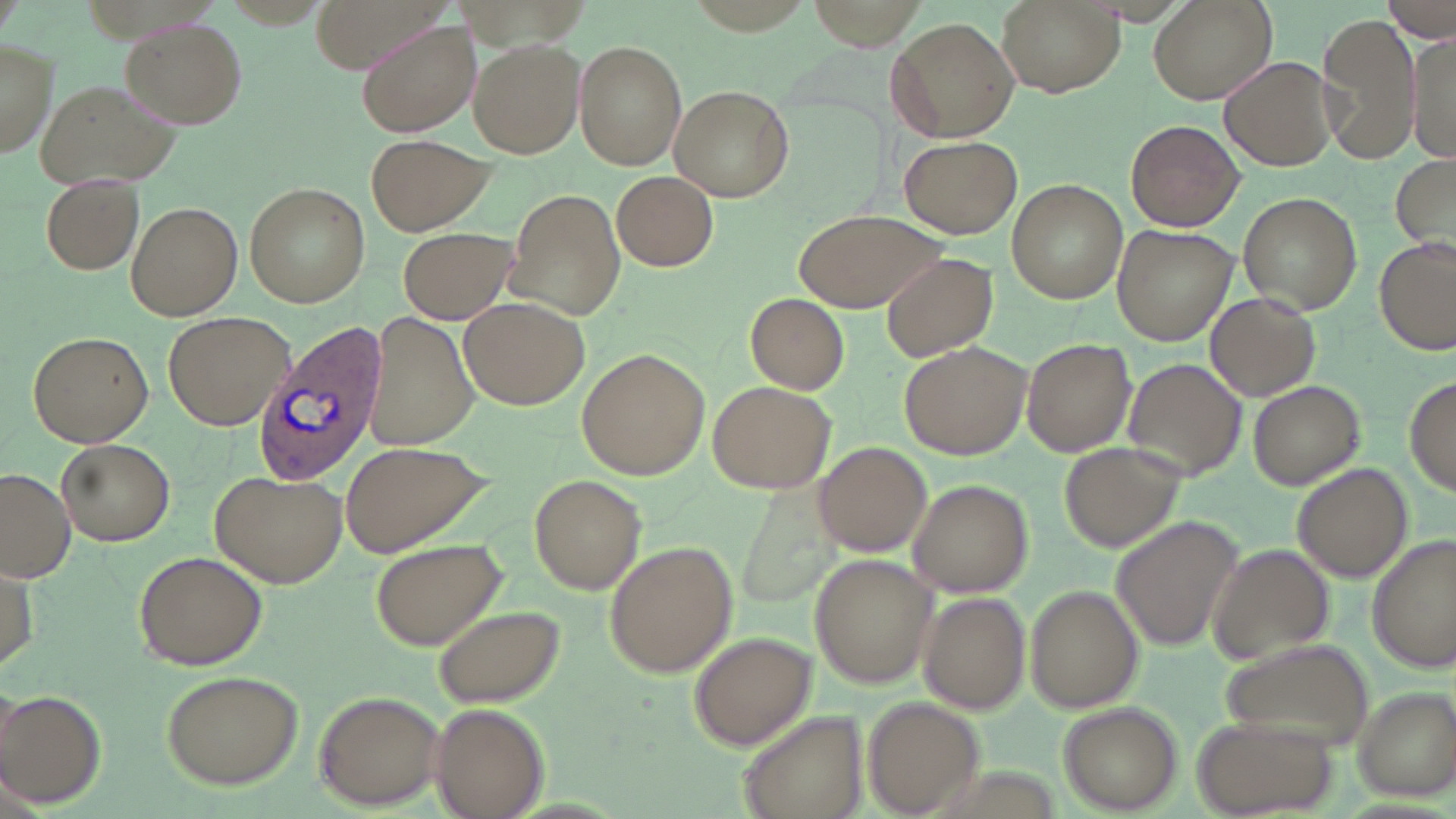

Summary:
  - Coordinate format: approximate bounding boxes as (x1,y1)-(x2,y2) corner pairs in pixels
  - Plasmodium ovale-infected red blood cell locations: (252,318)-(387,480)
  - Uninfected red blood cell locations: (308,0)-(450,75), (1147,0)-(1278,105), (1383,0)-(1455,44), (997,1)-(1123,97), (1317,11)-(1421,166), (886,16)-(1022,143), (123,17)-(247,128), (354,19)-(481,140), (1408,34)-(1454,164), (1,38)-(58,161), (467,38)-(587,159), (573,39)-(688,172), (1220,57)-(1337,172), (33,79)-(186,188), (668,85)-(794,202), (1125,120)-(1244,233), (364,135)-(493,235), (899,135)-(1021,239), (1391,153)-(1456,254), (611,170)-(719,273), (40,171)-(146,276), (1007,180)-(1128,304), (244,182)-(370,308), (506,185)-(625,321), (1238,191)-(1361,315), (128,200)-(242,321), (792,207)-(947,314), (1113,225)-(1238,346), (395,226)-(521,325), (1376,239)-(1453,355), (882,253)-(999,362), (745,294)-(849,394), (1207,294)-(1321,401), (460,296)-(590,408), (163,311)-(294,429), (366,313)-(481,450), (27,329)-(153,447), (1021,339)-(1135,457), (899,342)-(1030,457), (576,349)-(710,479), (1122,358)-(1246,479), (1406,377)-(1455,490), (707,380)-(835,496), (1248,380)-(1363,489), (55,438)-(175,547), (339,440)-(498,557), (813,441)-(932,556), (1058,442)-(1182,552), (1294,464)-(1414,582), (2,468)-(74,582), (211,469)-(346,588), (528,474)-(646,594), (908,478)-(1035,597), (742,482)-(842,607), (1112,517)-(1243,652), (369,537)-(511,653), (1370,538)-(1455,670), (604,541)-(737,678), (1207,544)-(1333,664), (133,549)-(267,671), (810,553)-(937,689), (1027,584)-(1143,714), (916,593)-(1028,714), (435,604)-(566,707), (688,632)-(817,748), (1216,638)-(1376,748), (159,670)-(303,788), (1348,687)-(1455,800), (1,690)-(104,809), (314,692)-(441,806), (864,699)-(983,815), (431,703)-(548,819), (1057,703)-(1180,813), (737,709)-(869,819), (1192,713)-(1338,816)
  - Slide-level diagnosis: Plasmodium ovale
  - Magnification: 1000x
  - Modality: light microscopy
  - Preparation: thin blood smear
  - Field of view: one of a larger specimen
  - Stain: May-Grünwald-Giemsa
  - Image size: 1456×819 pixels